Locate every uninfected red blood cell.
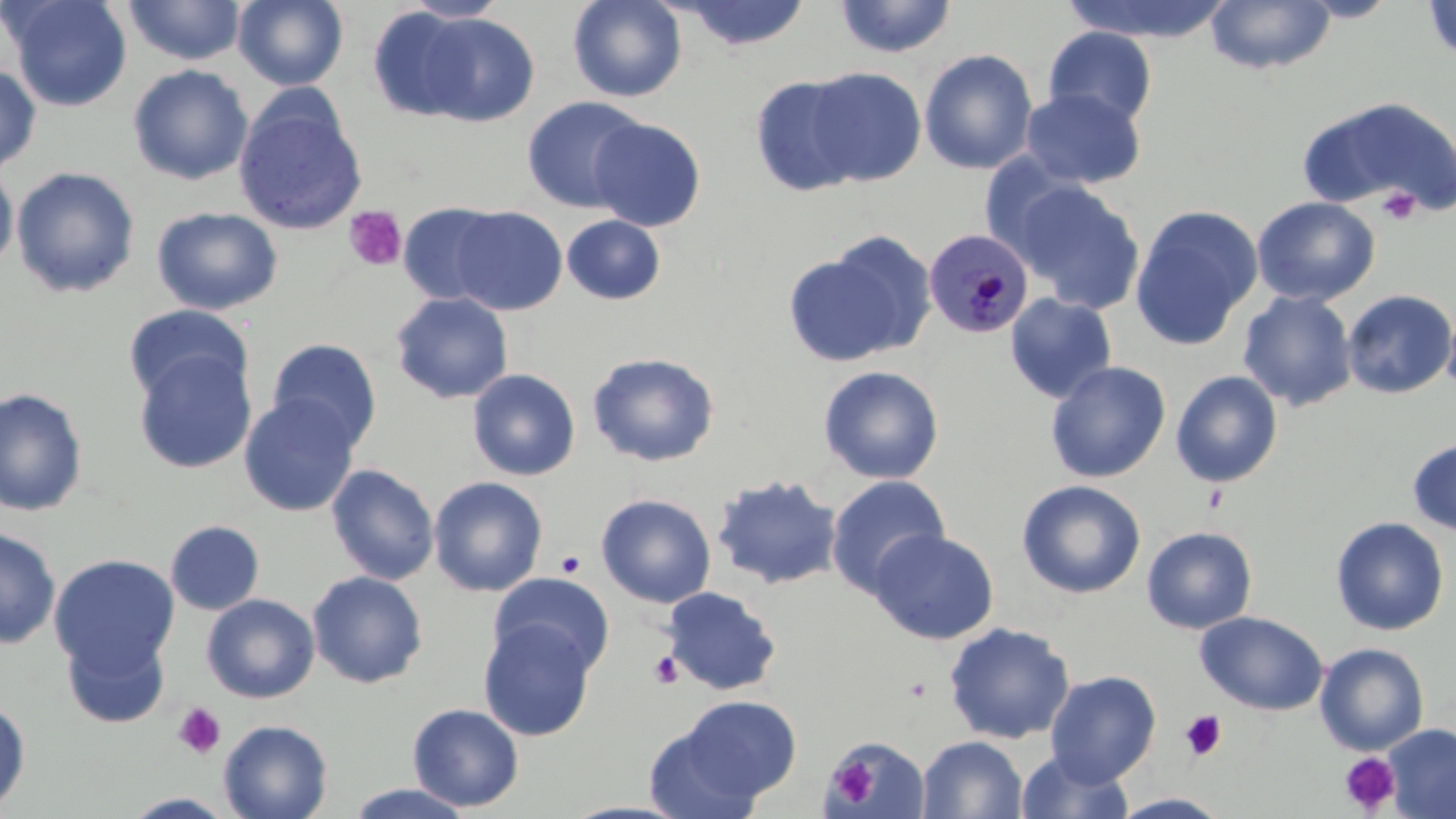
Approximate bounding boxes as (x1, y1, x2, y2) in pixels.
Uninfected red blood cells: (4, 0, 133, 112), (123, 0, 246, 65), (231, 0, 349, 91), (402, 0, 511, 22), (567, 0, 687, 103), (675, 0, 812, 51), (1061, 0, 1233, 43), (1298, 0, 1401, 22), (1422, 0, 1456, 64), (834, 1, 957, 59), (1205, 1, 1337, 75), (367, 7, 479, 122), (415, 12, 539, 126), (1043, 26, 1157, 128), (919, 49, 1038, 175), (0, 64, 41, 174), (127, 64, 253, 185), (804, 67, 927, 187), (749, 74, 867, 197), (1020, 87, 1145, 189), (234, 90, 368, 234), (520, 95, 649, 215), (1298, 95, 1455, 219), (588, 117, 706, 232), (0, 164, 19, 272), (11, 166, 140, 298), (1010, 179, 1145, 314), (1251, 196, 1380, 306), (398, 202, 508, 307), (449, 205, 568, 315), (1128, 205, 1264, 350), (151, 206, 284, 315), (562, 214, 666, 305), (785, 236, 932, 367), (1341, 289, 1456, 399), (1238, 291, 1358, 412), (390, 292, 514, 404), (1005, 293, 1117, 403), (1441, 300, 1456, 401), (123, 304, 253, 405), (266, 338, 382, 452), (132, 349, 257, 474), (587, 351, 720, 466), (1045, 361, 1171, 483), (818, 365, 944, 484), (467, 368, 581, 481), (1170, 370, 1284, 488), (0, 386, 88, 517), (238, 396, 360, 517), (1407, 437, 1456, 537), (326, 463, 440, 584), (711, 474, 843, 591), (825, 475, 950, 598), (428, 476, 548, 597), (1016, 479, 1146, 599), (596, 493, 717, 608), (1330, 516, 1449, 636), (164, 520, 265, 616), (1141, 526, 1258, 634), (0, 527, 60, 649), (869, 529, 998, 645), (48, 553, 180, 679), (307, 570, 428, 688), (488, 572, 615, 677), (661, 586, 782, 696), (201, 593, 320, 704), (1195, 611, 1328, 716), (478, 619, 597, 741), (943, 622, 1075, 744), (61, 627, 170, 729), (1314, 642, 1429, 756), (1045, 670, 1162, 785), (663, 695, 802, 808), (0, 697, 31, 813), (407, 703, 525, 812), (218, 719, 334, 819), (1384, 724, 1456, 819), (823, 735, 932, 819), (917, 735, 1028, 819), (1016, 748, 1134, 819), (346, 783, 475, 818), (120, 792, 238, 818), (1110, 793, 1233, 818), (557, 800, 695, 818).

slide-level diagnosis = Plasmodium malariae
platelet locations = approximate bounding boxes as (x1, y1, x2, y2) in pixels: (1377, 187, 1422, 225), (343, 205, 407, 271), (556, 551, 585, 578), (648, 650, 684, 689), (172, 703, 227, 759), (1179, 710, 1227, 760), (1338, 752, 1401, 815), (828, 758, 880, 803)
preparation = thin blood smear
stain = May-Grünwald-Giemsa
magnification = 1000x
modality = optical microscopy
field of view = single
Plasmodium malariae-infected red blood cell locations = approximate bounding boxes as (x1, y1, x2, y2) in pixels: (924, 229, 1033, 339)
image size = 1456×819 pixels